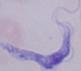

Summary:
  - Modality: photomicrograph
  - Identification: trypanosome
  - Magnification: 1000x